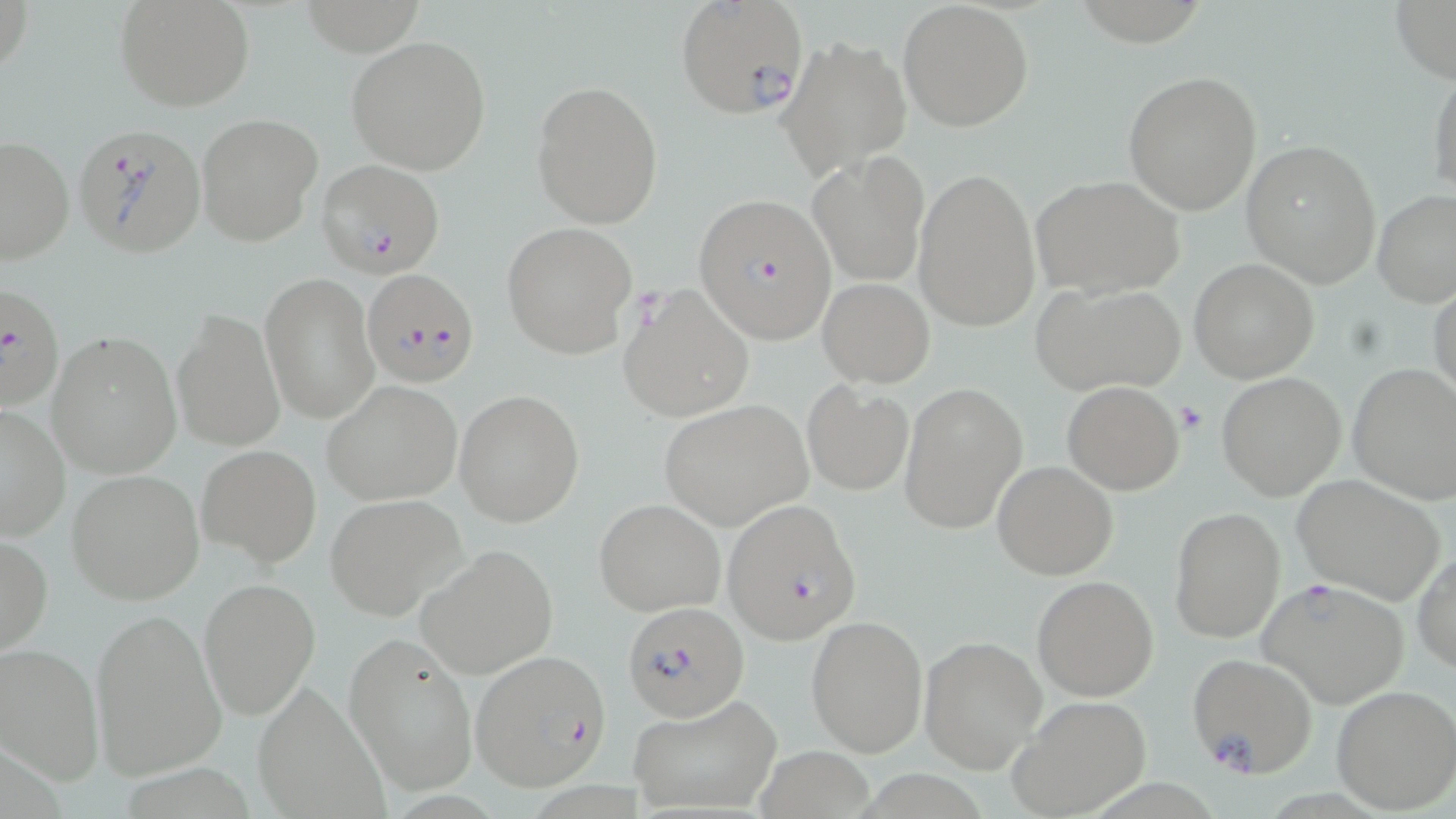
Summary:
  - Coordinate format: approximate bounding boxes as [x1, y1, x2, y2] in pixels
  - Plasmodium falciparum-infected red blood cell locations: [674, 0, 809, 121], [70, 122, 207, 258], [317, 160, 445, 277], [697, 193, 838, 347], [363, 269, 480, 388], [2, 283, 66, 415], [615, 283, 754, 423], [719, 498, 862, 644], [1259, 578, 1410, 709], [619, 599, 747, 719], [469, 650, 610, 789], [1187, 652, 1318, 778]
  - Platelet locations: [1176, 403, 1208, 434]
  - Uninfected red blood cell locations: [113, 0, 257, 112], [1390, 0, 1456, 86], [898, 2, 1034, 131], [777, 33, 912, 176], [345, 35, 492, 174], [1428, 66, 1456, 205], [1122, 69, 1263, 216], [531, 80, 663, 229], [196, 112, 323, 249], [1, 134, 75, 265], [1241, 140, 1382, 286], [808, 151, 930, 287], [913, 166, 1042, 333], [1030, 175, 1186, 298], [1373, 190, 1456, 308], [502, 220, 637, 358], [1189, 259, 1319, 383], [260, 273, 379, 424], [818, 277, 934, 386], [1031, 281, 1185, 395], [1430, 281, 1455, 407], [172, 311, 284, 452], [48, 330, 182, 478], [1346, 363, 1456, 506], [1217, 372, 1346, 500], [321, 379, 464, 505], [801, 379, 914, 496], [900, 380, 1027, 534], [1062, 381, 1184, 495], [454, 390, 585, 526], [658, 398, 813, 530], [0, 403, 71, 540], [197, 444, 322, 568], [992, 459, 1118, 579], [66, 469, 205, 604], [1292, 475, 1448, 605], [325, 493, 466, 620], [595, 498, 726, 617], [1170, 507, 1287, 644], [0, 533, 51, 657], [416, 544, 558, 678], [1412, 549, 1456, 674], [1032, 575, 1159, 701], [199, 577, 321, 720], [89, 608, 226, 781], [805, 616, 929, 757], [344, 633, 476, 796], [919, 634, 1045, 776], [0, 642, 103, 783], [251, 681, 390, 819], [1330, 685, 1456, 813], [630, 693, 780, 814], [1009, 696, 1151, 818], [754, 748, 874, 818]
  - Slide-level diagnosis: Plasmodium falciparum
  - Preparation: thin blood smear
  - Image size: 1456×819 pixels
  - Field of view: single
  - Magnification: 1000x
  - Stain: May-Grünwald-Giemsa
  - Modality: light microscopy